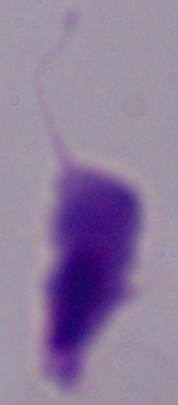
Captured at 1000x magnification. A trichomonad is seen. Photomicrograph.